Outline each uninfected red blood cell.
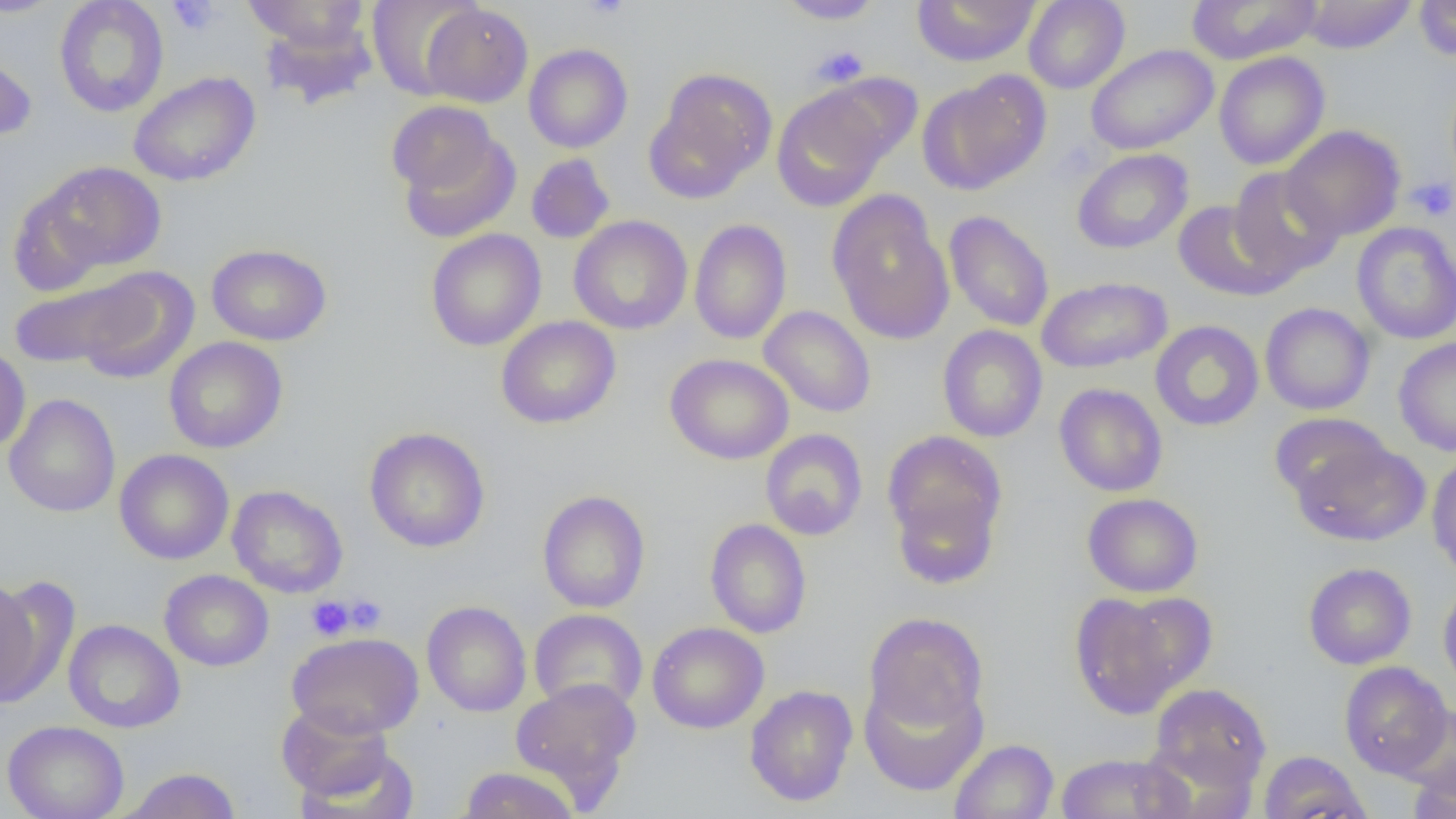
Approximate bounding boxes as named x1/y1/x2/y2 corners in pixels.
Uninfected red blood cells: (x1=0, y1=0, x2=65, y2=18), (x1=54, y1=0, x2=169, y2=117), (x1=242, y1=0, x2=369, y2=49), (x1=367, y1=0, x2=485, y2=100), (x1=776, y1=0, x2=884, y2=24), (x1=912, y1=0, x2=1040, y2=67), (x1=1023, y1=0, x2=1130, y2=93), (x1=1186, y1=0, x2=1323, y2=65), (x1=1298, y1=0, x2=1417, y2=53), (x1=1414, y1=0, x2=1456, y2=61), (x1=421, y1=3, x2=533, y2=107), (x1=260, y1=15, x2=377, y2=110), (x1=0, y1=44, x2=37, y2=142), (x1=524, y1=44, x2=633, y2=153), (x1=1086, y1=44, x2=1218, y2=155), (x1=1214, y1=51, x2=1330, y2=170), (x1=647, y1=68, x2=777, y2=200), (x1=128, y1=71, x2=261, y2=187), (x1=919, y1=72, x2=1051, y2=195), (x1=819, y1=73, x2=922, y2=167), (x1=771, y1=85, x2=890, y2=212), (x1=393, y1=117, x2=520, y2=244), (x1=1281, y1=125, x2=1406, y2=241), (x1=1071, y1=148, x2=1193, y2=254), (x1=526, y1=154, x2=615, y2=244), (x1=24, y1=161, x2=167, y2=280), (x1=1228, y1=167, x2=1343, y2=283), (x1=828, y1=194, x2=954, y2=345), (x1=1173, y1=200, x2=1289, y2=300), (x1=944, y1=211, x2=1054, y2=332), (x1=568, y1=215, x2=693, y2=335), (x1=689, y1=219, x2=792, y2=345), (x1=1351, y1=222, x2=1456, y2=345), (x1=426, y1=229, x2=546, y2=351), (x1=206, y1=243, x2=332, y2=346), (x1=74, y1=267, x2=199, y2=385), (x1=7, y1=273, x2=154, y2=371), (x1=1036, y1=276, x2=1173, y2=374), (x1=1260, y1=302, x2=1375, y2=415), (x1=759, y1=306, x2=876, y2=418), (x1=496, y1=316, x2=621, y2=429), (x1=1150, y1=320, x2=1264, y2=432), (x1=937, y1=324, x2=1048, y2=442), (x1=163, y1=337, x2=288, y2=453), (x1=1393, y1=337, x2=1456, y2=456), (x1=0, y1=344, x2=30, y2=453), (x1=665, y1=353, x2=794, y2=464), (x1=1054, y1=383, x2=1168, y2=497), (x1=4, y1=393, x2=121, y2=518), (x1=1269, y1=412, x2=1391, y2=506), (x1=364, y1=427, x2=490, y2=552), (x1=760, y1=429, x2=868, y2=541), (x1=883, y1=430, x2=1007, y2=557), (x1=1290, y1=436, x2=1429, y2=547), (x1=114, y1=449, x2=234, y2=564), (x1=1427, y1=454, x2=1456, y2=578), (x1=227, y1=484, x2=348, y2=598), (x1=890, y1=485, x2=1003, y2=589), (x1=537, y1=490, x2=651, y2=613), (x1=1082, y1=493, x2=1203, y2=597), (x1=704, y1=519, x2=811, y2=638), (x1=1303, y1=562, x2=1417, y2=669), (x1=159, y1=569, x2=273, y2=671), (x1=0, y1=578, x2=46, y2=706), (x1=1438, y1=580, x2=1456, y2=694), (x1=1069, y1=592, x2=1188, y2=719), (x1=1115, y1=592, x2=1218, y2=695), (x1=422, y1=600, x2=532, y2=717), (x1=529, y1=609, x2=648, y2=714), (x1=864, y1=612, x2=988, y2=732), (x1=63, y1=619, x2=185, y2=733), (x1=647, y1=622, x2=769, y2=734), (x1=287, y1=632, x2=424, y2=739), (x1=1339, y1=661, x2=1453, y2=778), (x1=859, y1=674, x2=988, y2=796), (x1=510, y1=677, x2=642, y2=804), (x1=1149, y1=683, x2=1272, y2=792), (x1=744, y1=685, x2=858, y2=807), (x1=277, y1=703, x2=392, y2=800), (x1=1395, y1=704, x2=1456, y2=797), (x1=2, y1=720, x2=129, y2=819), (x1=470, y1=731, x2=619, y2=807), (x1=949, y1=739, x2=1058, y2=819), (x1=296, y1=747, x2=418, y2=819), (x1=1257, y1=750, x2=1371, y2=819), (x1=1055, y1=752, x2=1189, y2=818), (x1=1408, y1=762, x2=1455, y2=819), (x1=458, y1=766, x2=580, y2=819), (x1=120, y1=767, x2=241, y2=818).

slide-level diagnosis = no evidence of blood parasites
preparation = thin blood smear
field of view = one of a larger specimen
platelet locations = approximate bounding boxes as named x1/y1/x2/y2 corners in pixels: (x1=167, y1=0, x2=221, y2=36), (x1=580, y1=0, x2=630, y2=20), (x1=812, y1=45, x2=868, y2=87), (x1=1408, y1=177, x2=1455, y2=222), (x1=341, y1=595, x2=387, y2=635), (x1=306, y1=596, x2=355, y2=641)
modality = optical microscopy
image size = 1456×819 pixels
magnification = 1000x